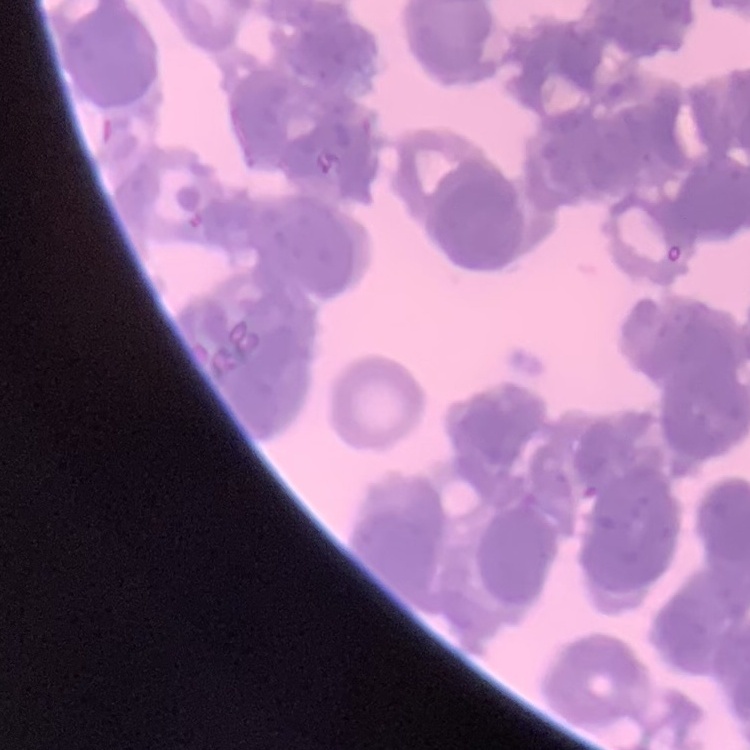
The erythrocytes show rouleaux formation. Stained with either Field's or Giemsa. Thin peripheral smear. One tile cut from a larger photomicrograph.